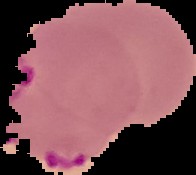

Summary:
  - Preparation: thin blood film
  - Result: Plasmodium parasites identified
  - Image type: segmented cell region with the area outside set to black
  - Image size: 196×175 pixels